Describe the morphology of the erythrocytes.
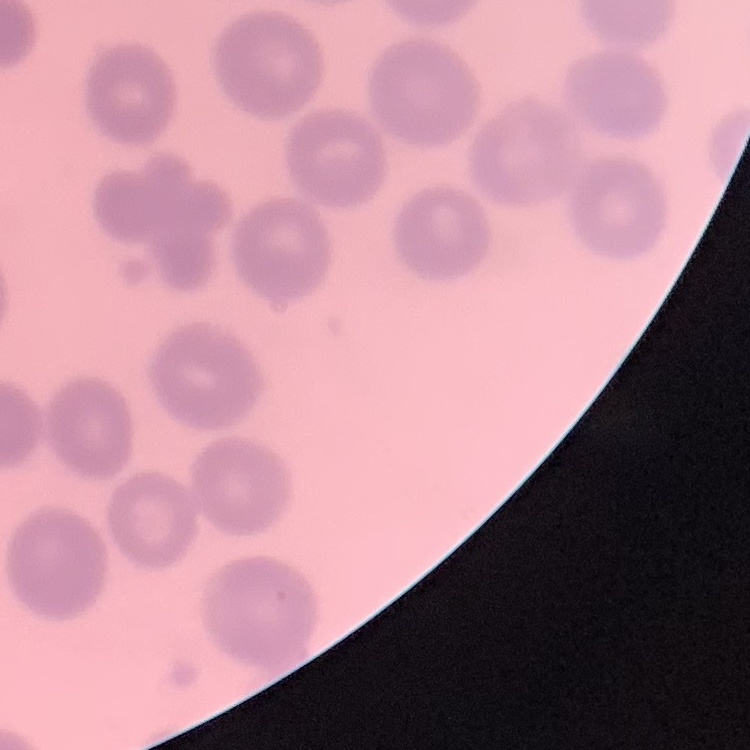
They show no rouleaux formation.

One tile cut from a larger photomicrograph. Stained with either Field's or Giemsa. Thin peripheral smear.